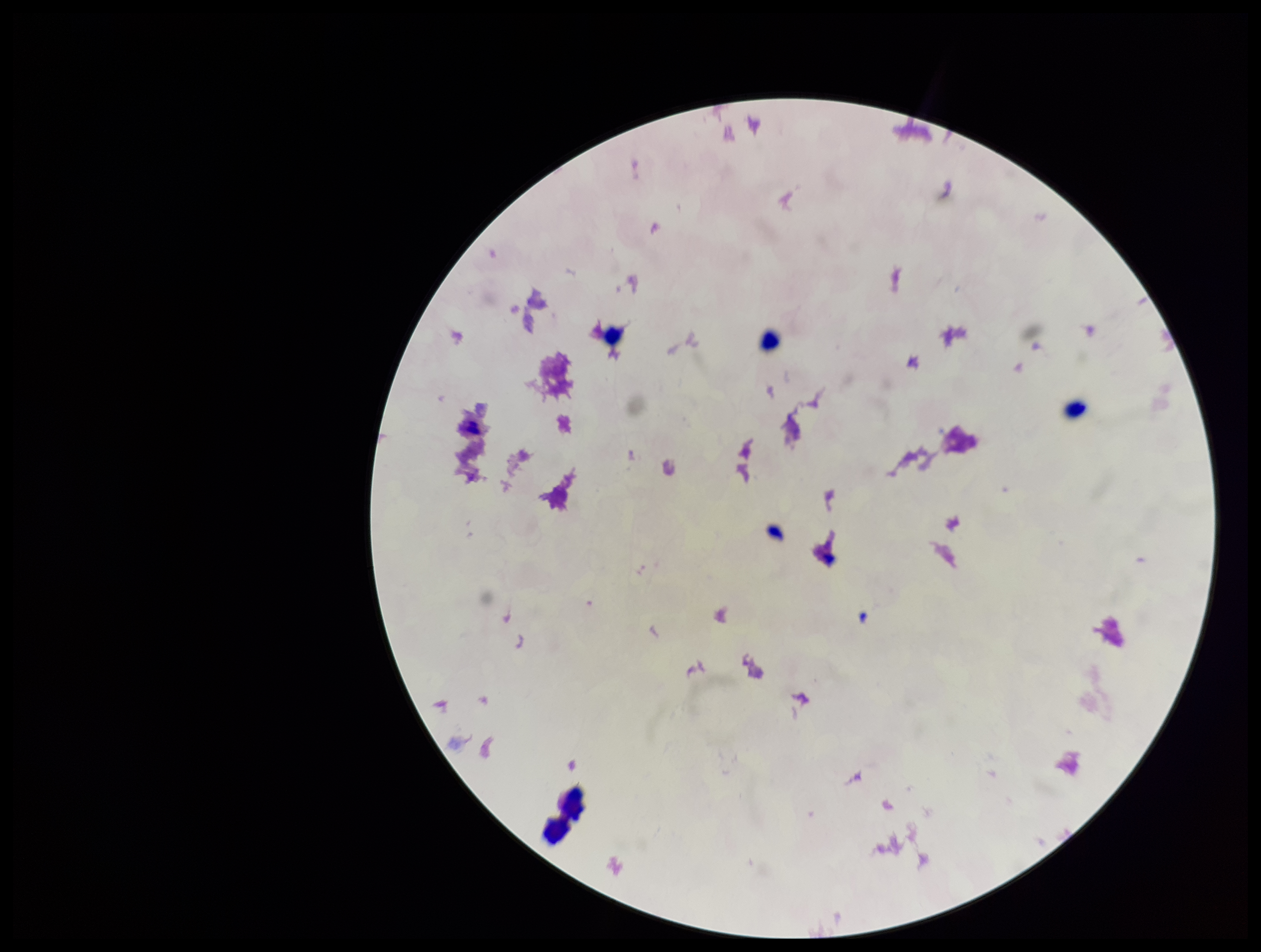
Summary:
  - Capture: smartphone photograph through the microscope eyepiece
  - Leukocyte count: 3
  - Field of view: one from this slide
  - Parasite count: 0
  - Preparation: thick smear
  - Image size: 1261×952 pixels
  - Patient malaria status: negative
  - Plasmodium parasites: none seen
  - Stain: Giemsa